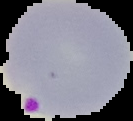

{
  "image_type": "segmented cell region with the area outside set to black",
  "preparation": "thin blood smear",
  "result": "malaria parasites identified",
  "image_size": "133×121 pixels"
}